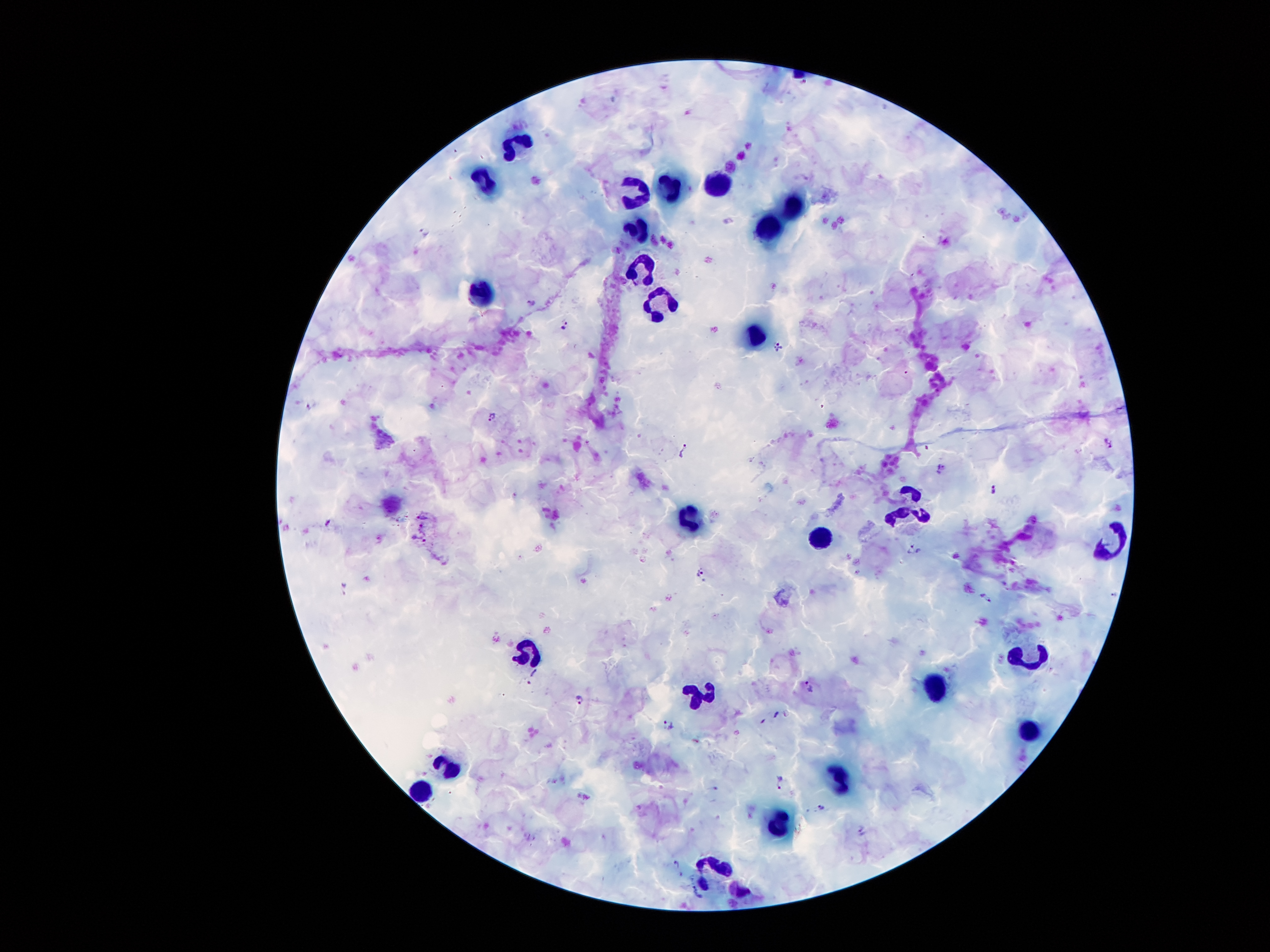
Approximate centers as [x, y] in pixels.
Summary:
  - Plasmodium parasite locations: [426, 232], [532, 303], [565, 327], [778, 347], [312, 405], [492, 417], [1108, 442], [686, 453], [942, 470], [994, 491], [914, 552], [703, 573], [1114, 595], [985, 597], [810, 686], [580, 700], [778, 716], [670, 726], [781, 782], [823, 808], [677, 865], [691, 895]
  - Leukocyte locations: [512, 146], [483, 179], [717, 182], [665, 189], [629, 192], [795, 200], [640, 225], [767, 228], [641, 271], [486, 294], [662, 302], [759, 334], [906, 504], [687, 518], [1113, 539], [816, 541], [522, 649], [1030, 658], [931, 681], [699, 700], [1033, 735], [451, 763], [840, 781], [421, 786], [774, 831], [718, 872]
  - Stain: Giemsa
  - Image size: 1270×952 pixels
  - Magnification: 100x
  - Field of view: one from this slide
  - Capture: smartphone through the microscope eyepiece
  - Patient malaria status: positive for Plasmodium falciparum
  - Preparation: thick blood smear